Comment on the morphology of the red blood cells.
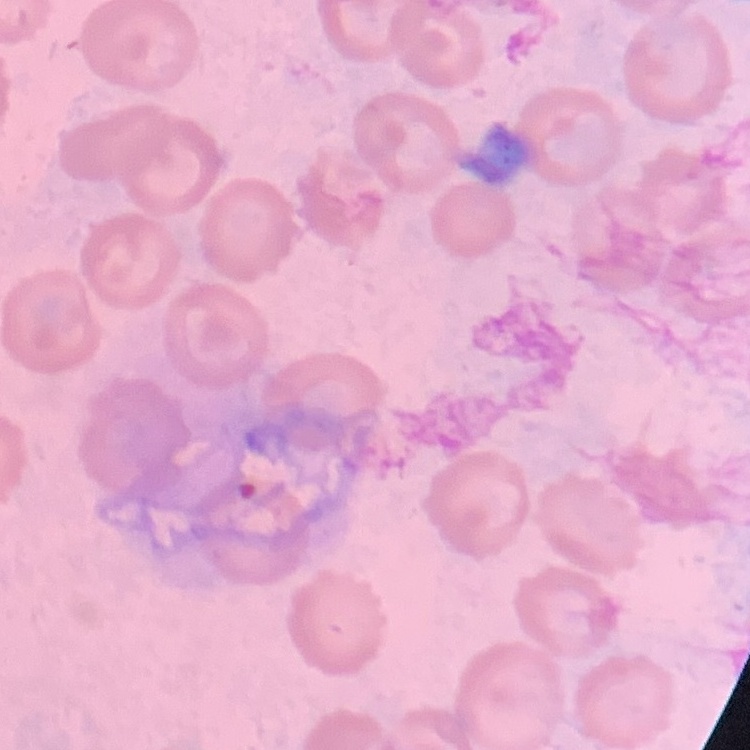
They show no rouleaux formation.

Field's or Giemsa stain. Square crop of a larger photomicrograph. Thin peripheral smear.